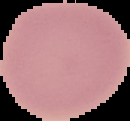

From a thin blood film. The area outside the segmented cell region is set to black. Image is 130×121 pixels. Malaria status: uninfected.